Describe the morphology of the red blood cells.
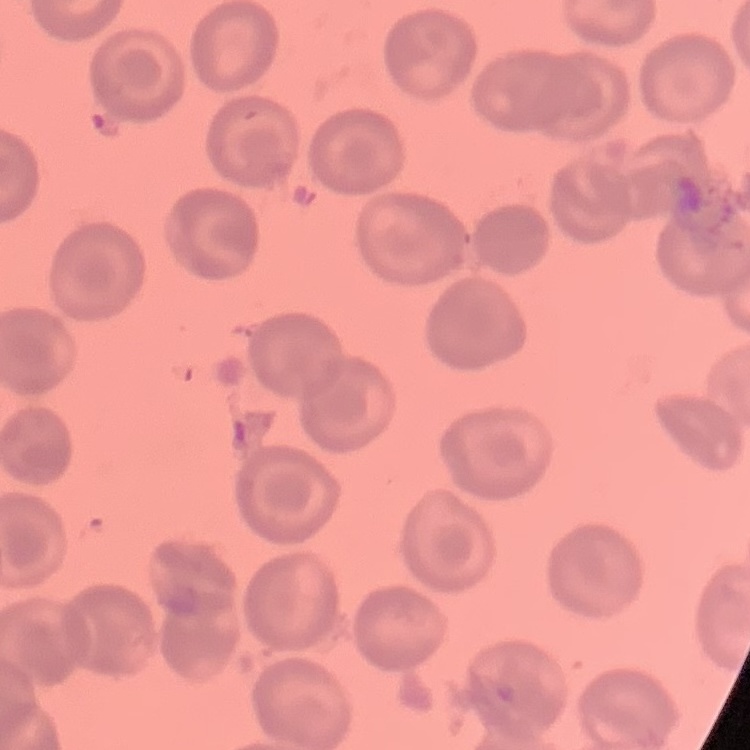
They show no rouleaux formation.

Square crop of a larger photomicrograph. Thin blood smear. Stained with either Field's or Giemsa.